Locate every Plasmodium parasite.
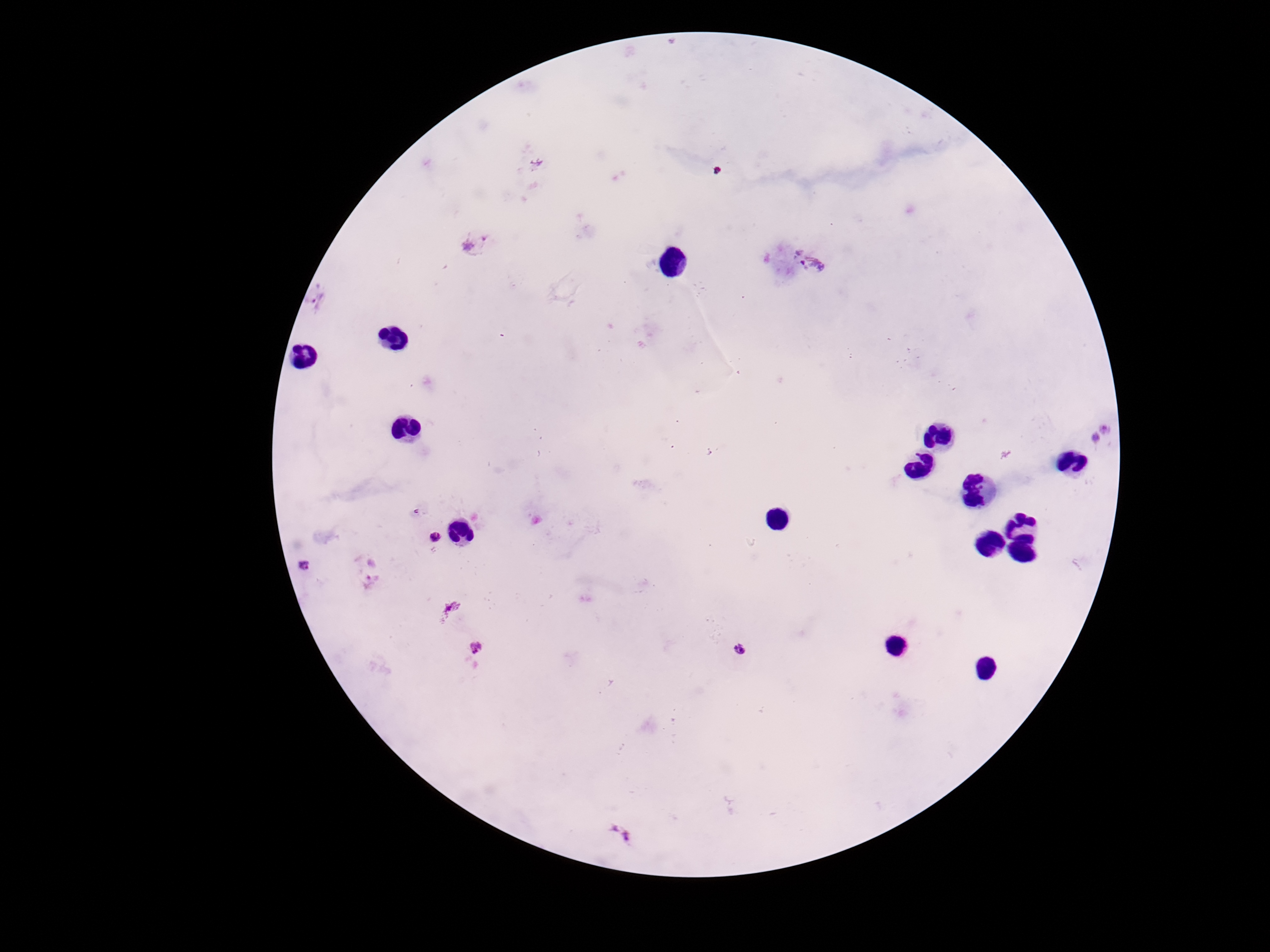

Approximate centers as {x, y} in pixels.
Plasmodium parasites: {472, 244}, {811, 262}, {318, 299}, {1101, 434}, {433, 536}, {304, 566}, {369, 570}, {452, 608}, {475, 647}, {743, 651}, {617, 834}.

Summary:
  - Stain: Giemsa
  - Patient malaria status: positive
  - Magnification: 100x
  - Capture: smartphone camera through the microscope eyepiece
  - Field of view: one from this slide
  - Image size: 1270×952 pixels
  - Preparation: thick peripheral-blood smear